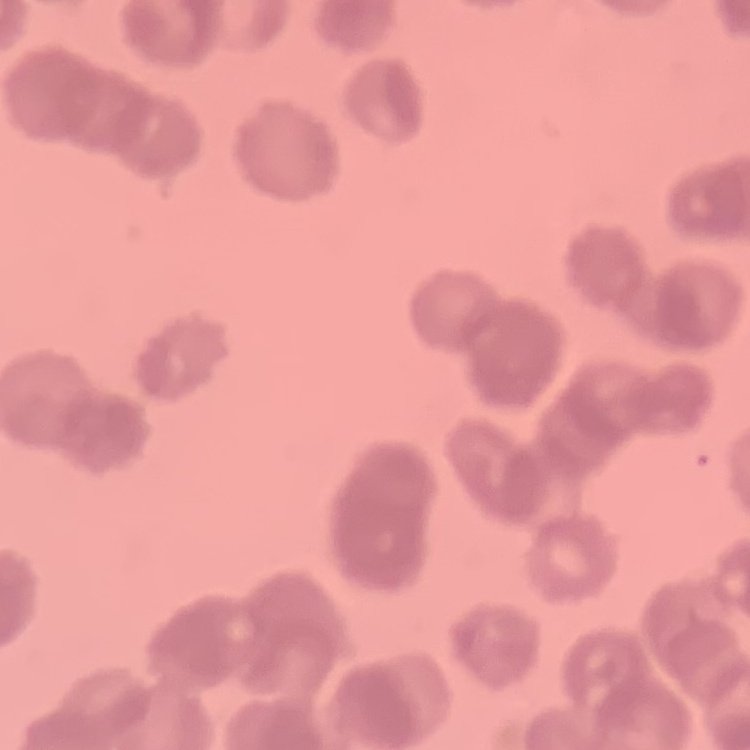

The red blood cells show rouleaux formation. Square crop of a larger photomicrograph. Thin blood smear. Field's or Giemsa stain.